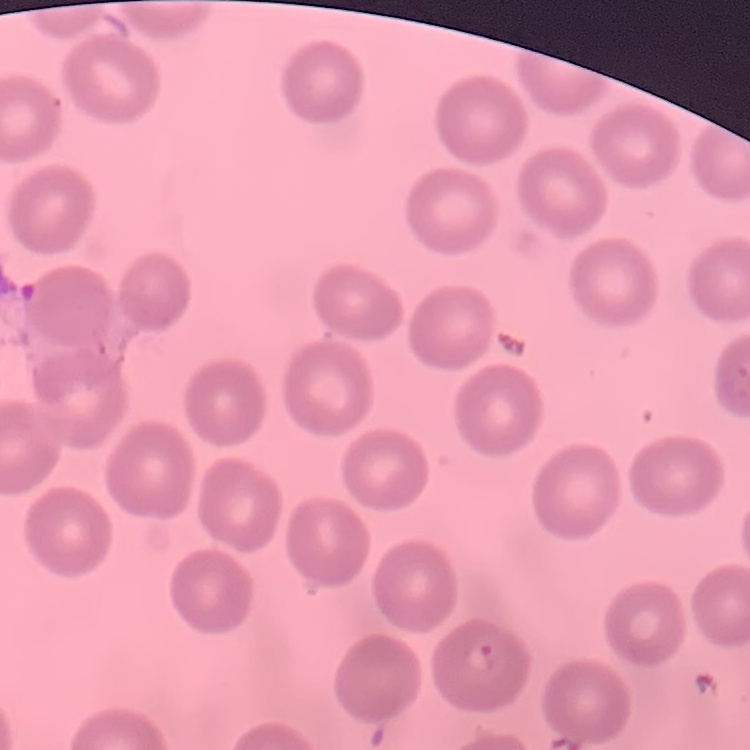

The red blood cells show no rouleaux formation. Stained with either Field's or Giemsa. One tile cut from a larger photomicrograph. Thin peripheral smear.